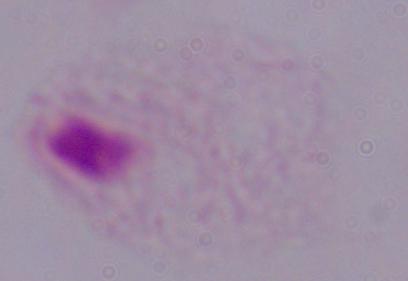

modality = photomicrograph
magnification = 1000x
identification = trichomonad